Comment on the morphology of the red blood cells.
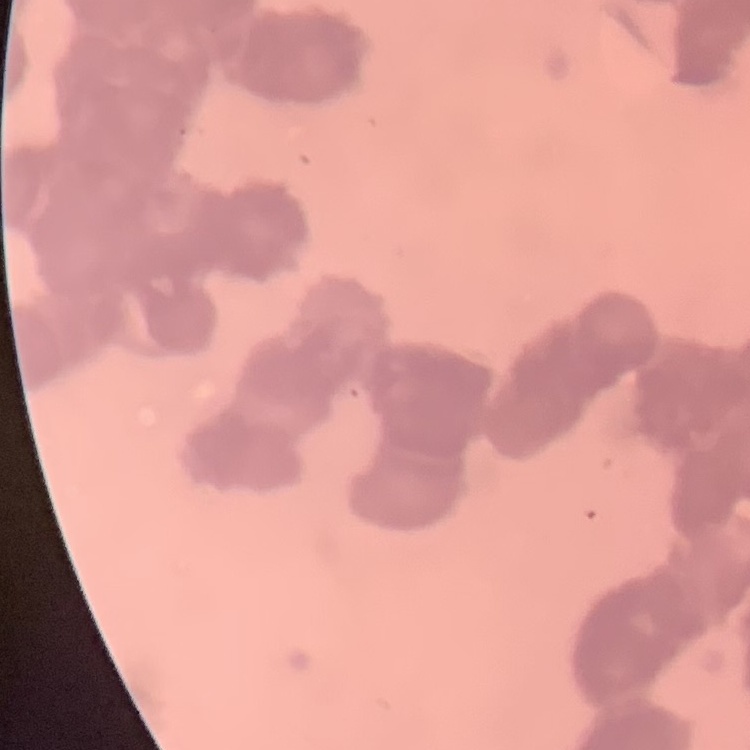

Rouleaux formation.

Summary:
  - Stain: Field's or Giemsa
  - Preparation: thin blood smear
  - Image type: one tile cut from a larger photomicrograph